State which parasite is depicted.
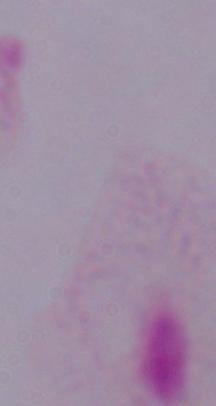
A trichomonad.

Summary:
  - Magnification: 1000x
  - Modality: micrograph